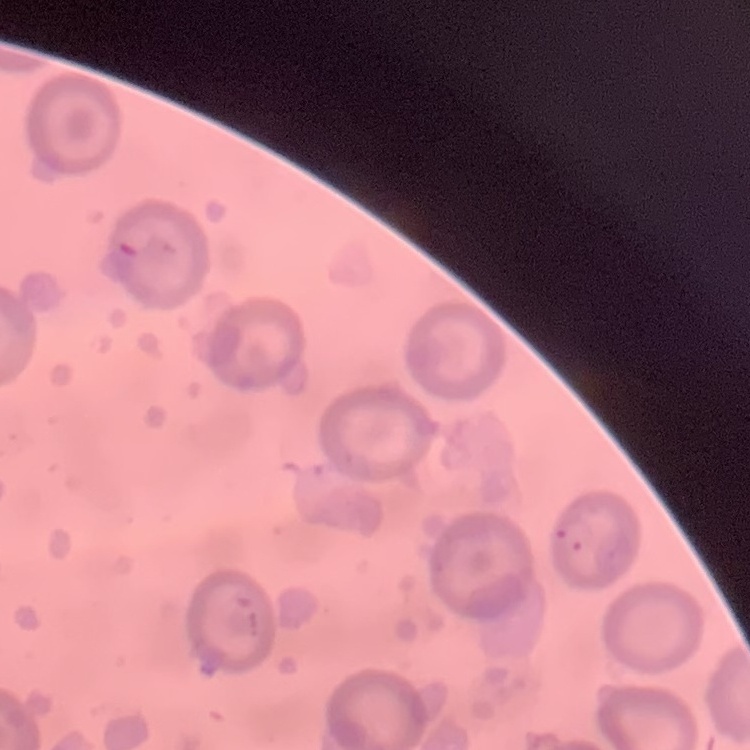
The erythrocytes exhibit no rouleaux formation. Field's or Giemsa stain. Thin blood smear. Square crop of a larger photomicrograph.